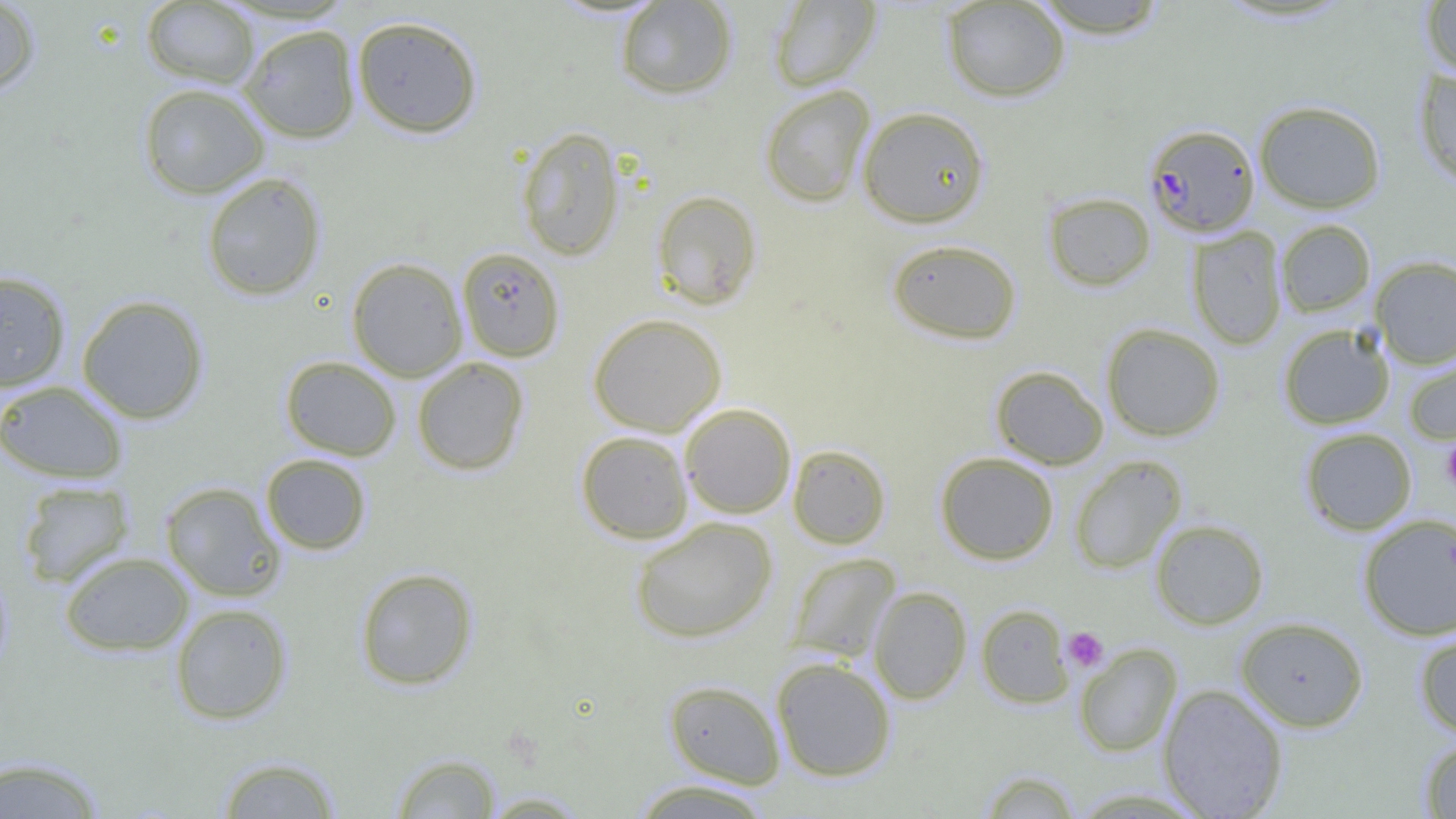

Summary:
  - Coordinate format: approximate bounding boxes as named x1/y1/x2/y2 corners in pixels
  - Uninfected red blood cell locations: (x1=0, y1=0, x2=41, y2=98), (x1=1029, y1=0, x2=1171, y2=38), (x1=141, y1=1, x2=259, y2=87), (x1=614, y1=1, x2=738, y2=100), (x1=769, y1=1, x2=880, y2=91), (x1=941, y1=1, x2=1070, y2=102), (x1=1421, y1=1, x2=1456, y2=80), (x1=351, y1=15, x2=483, y2=138), (x1=239, y1=24, x2=360, y2=143), (x1=1414, y1=67, x2=1456, y2=189), (x1=137, y1=82, x2=269, y2=199), (x1=759, y1=85, x2=875, y2=207), (x1=1254, y1=100, x2=1386, y2=214), (x1=857, y1=106, x2=990, y2=228), (x1=516, y1=126, x2=625, y2=262), (x1=201, y1=172, x2=326, y2=301), (x1=651, y1=190, x2=762, y2=310), (x1=1043, y1=192, x2=1156, y2=291), (x1=1275, y1=219, x2=1375, y2=317), (x1=1187, y1=226, x2=1287, y2=350), (x1=886, y1=238, x2=1022, y2=345), (x1=456, y1=247, x2=565, y2=362), (x1=1370, y1=256, x2=1456, y2=369), (x1=346, y1=257, x2=468, y2=381), (x1=0, y1=270, x2=71, y2=392), (x1=77, y1=294, x2=210, y2=424), (x1=588, y1=313, x2=727, y2=436), (x1=1101, y1=323, x2=1226, y2=441), (x1=1278, y1=324, x2=1394, y2=429), (x1=1403, y1=350, x2=1456, y2=445), (x1=280, y1=356, x2=401, y2=460), (x1=411, y1=357, x2=529, y2=476), (x1=991, y1=365, x2=1108, y2=470), (x1=0, y1=380, x2=129, y2=484), (x1=679, y1=403, x2=796, y2=518), (x1=1300, y1=427, x2=1417, y2=535), (x1=576, y1=431, x2=694, y2=544), (x1=787, y1=444, x2=891, y2=549), (x1=935, y1=452, x2=1059, y2=564), (x1=260, y1=454, x2=372, y2=555), (x1=1068, y1=455, x2=1186, y2=574), (x1=17, y1=480, x2=135, y2=588), (x1=160, y1=481, x2=286, y2=602), (x1=630, y1=517, x2=778, y2=643), (x1=1354, y1=517, x2=1456, y2=650), (x1=1150, y1=518, x2=1269, y2=629), (x1=59, y1=551, x2=193, y2=656), (x1=787, y1=552, x2=901, y2=664), (x1=0, y1=563, x2=14, y2=682), (x1=355, y1=567, x2=478, y2=690), (x1=869, y1=586, x2=972, y2=704), (x1=170, y1=603, x2=293, y2=725), (x1=976, y1=604, x2=1073, y2=708), (x1=1235, y1=616, x2=1368, y2=732), (x1=1413, y1=627, x2=1456, y2=739), (x1=1074, y1=644, x2=1182, y2=756), (x1=771, y1=657, x2=896, y2=782), (x1=664, y1=679, x2=785, y2=788), (x1=1157, y1=684, x2=1288, y2=818), (x1=1419, y1=737, x2=1456, y2=818), (x1=390, y1=752, x2=503, y2=818), (x1=0, y1=754, x2=108, y2=818), (x1=216, y1=755, x2=342, y2=818), (x1=978, y1=769, x2=1081, y2=818), (x1=629, y1=779, x2=775, y2=818), (x1=478, y1=791, x2=592, y2=817)
  - Platelet locations: (x1=1441, y1=440, x2=1456, y2=494), (x1=1064, y1=627, x2=1108, y2=672)
  - Plasmodium falciparum-infected red blood cell locations: (x1=1144, y1=123, x2=1260, y2=236)
  - Slide-level diagnosis: Plasmodium falciparum
  - Field of view: one of a larger specimen
  - Preparation: thin blood smear
  - Image size: 1456×819 pixels
  - Modality: light microscopy
  - Magnification: 1000x